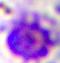
modality = micrograph
magnification = 400x
identification = leukocyte